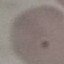
Malaria status: uninfected. Automatically extracted cell patch, resized to 64 × 64 pixels. Giemsa stain. Thin blood film. Photographed with a smartphone camera at the microscope eyepiece.